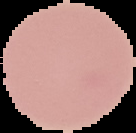
malaria_status: uninfected
image_type: cell region segmented out of the field of view; surrounding area masked to black
image_size: 136×133 pixels
preparation: thin blood smear